Classify this cell by malaria status.
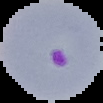

Parasitized.

From a thin blood film. Cell region segmented out of the field of view; the surrounding area is masked to black. Image is 103×103 pixels.